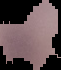
Summary:
  - Result: no malaria parasites seen
  - Image type: cell region segmented out of the field of view; surrounding area masked to black
  - Preparation: thin blood film
  - Image size: 61×70 pixels